Classify this cell by malaria status.
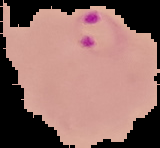
It is parasitized.

The area outside the segmented cell region is set to black. From a thin blood film. Image is 160×148 pixels.